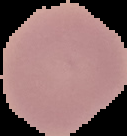

Summary:
  - Malaria status: uninfected
  - Image size: 127×136 pixels
  - Image type: cell region segmented out of the field of view; surrounding area masked to black
  - Preparation: thin blood film